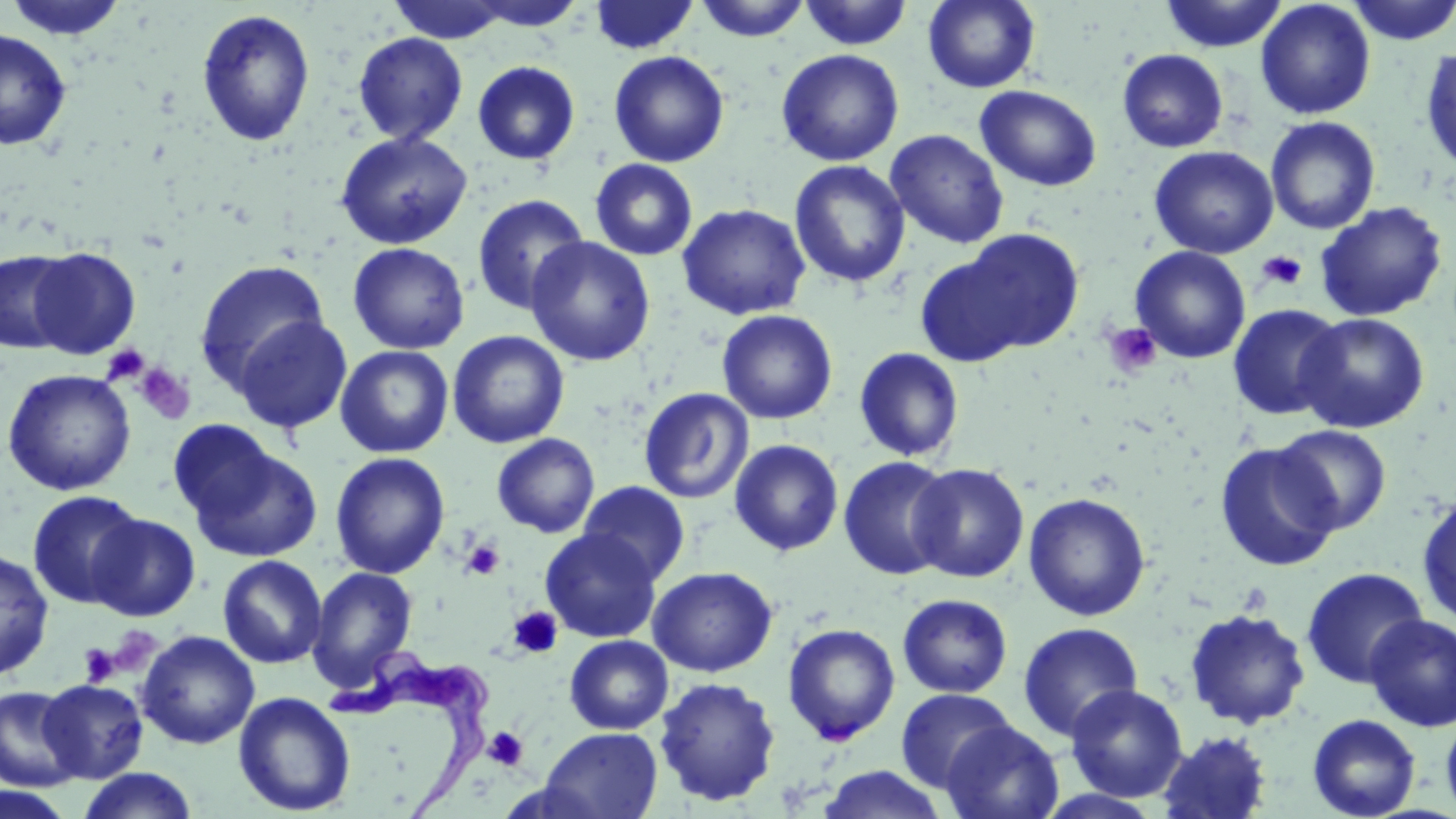

Summary:
  - Coordinate format: approximate bounding boxes as named x1/y1/x2/y2 corners in pixels
  - Platelet locations: (x1=1256, y1=250, x2=1308, y2=291), (x1=1103, y1=322, x2=1163, y2=378), (x1=102, y1=344, x2=150, y2=387), (x1=134, y1=362, x2=195, y2=424), (x1=462, y1=539, x2=504, y2=580), (x1=508, y1=606, x2=563, y2=659), (x1=106, y1=625, x2=163, y2=676), (x1=79, y1=643, x2=120, y2=686), (x1=483, y1=726, x2=529, y2=771)
  - Uninfected red blood cell locations: (x1=4, y1=0, x2=131, y2=41), (x1=386, y1=0, x2=516, y2=44), (x1=461, y1=0, x2=588, y2=31), (x1=589, y1=0, x2=700, y2=55), (x1=694, y1=0, x2=811, y2=41), (x1=798, y1=0, x2=913, y2=50), (x1=923, y1=0, x2=1040, y2=93), (x1=1159, y1=0, x2=1288, y2=53), (x1=1255, y1=0, x2=1376, y2=120), (x1=1345, y1=0, x2=1455, y2=45), (x1=196, y1=8, x2=316, y2=148), (x1=0, y1=28, x2=72, y2=151), (x1=353, y1=32, x2=467, y2=145), (x1=1420, y1=44, x2=1456, y2=174), (x1=776, y1=49, x2=904, y2=166), (x1=1117, y1=49, x2=1229, y2=152), (x1=608, y1=50, x2=729, y2=167), (x1=472, y1=61, x2=581, y2=166), (x1=975, y1=84, x2=1101, y2=192), (x1=1265, y1=117, x2=1381, y2=234), (x1=885, y1=129, x2=1009, y2=249), (x1=334, y1=130, x2=472, y2=250), (x1=1149, y1=146, x2=1279, y2=259), (x1=590, y1=158, x2=698, y2=260), (x1=789, y1=160, x2=911, y2=288), (x1=471, y1=194, x2=590, y2=316), (x1=1315, y1=201, x2=1449, y2=322), (x1=677, y1=203, x2=811, y2=320), (x1=952, y1=229, x2=1086, y2=355), (x1=526, y1=236, x2=655, y2=366), (x1=348, y1=242, x2=469, y2=354), (x1=1129, y1=245, x2=1251, y2=364), (x1=27, y1=246, x2=141, y2=359), (x1=0, y1=249, x2=75, y2=354), (x1=914, y1=252, x2=1036, y2=367), (x1=194, y1=259, x2=330, y2=392), (x1=1227, y1=304, x2=1346, y2=420), (x1=716, y1=309, x2=838, y2=424), (x1=1297, y1=312, x2=1429, y2=433), (x1=233, y1=315, x2=353, y2=434), (x1=448, y1=330, x2=570, y2=449), (x1=335, y1=344, x2=454, y2=458), (x1=853, y1=347, x2=965, y2=462), (x1=1, y1=368, x2=137, y2=496), (x1=639, y1=387, x2=754, y2=504), (x1=1273, y1=425, x2=1392, y2=534), (x1=492, y1=433, x2=599, y2=538), (x1=178, y1=434, x2=324, y2=563), (x1=729, y1=439, x2=844, y2=556), (x1=1214, y1=441, x2=1342, y2=572), (x1=330, y1=452, x2=450, y2=579), (x1=838, y1=455, x2=955, y2=580), (x1=908, y1=463, x2=1029, y2=582), (x1=578, y1=480, x2=691, y2=585), (x1=27, y1=490, x2=145, y2=609), (x1=1023, y1=492, x2=1151, y2=621), (x1=1416, y1=495, x2=1456, y2=628), (x1=88, y1=514, x2=201, y2=621), (x1=540, y1=528, x2=661, y2=643), (x1=0, y1=547, x2=54, y2=679), (x1=217, y1=554, x2=327, y2=668), (x1=307, y1=566, x2=419, y2=692), (x1=647, y1=566, x2=777, y2=677), (x1=1300, y1=566, x2=1429, y2=688), (x1=897, y1=594, x2=1013, y2=698), (x1=1184, y1=608, x2=1312, y2=729), (x1=1363, y1=614, x2=1456, y2=732), (x1=1017, y1=622, x2=1143, y2=743), (x1=782, y1=623, x2=901, y2=745), (x1=137, y1=630, x2=259, y2=749), (x1=564, y1=635, x2=673, y2=734), (x1=654, y1=676, x2=781, y2=806), (x1=38, y1=679, x2=148, y2=783), (x1=1066, y1=684, x2=1188, y2=802), (x1=0, y1=686, x2=82, y2=792), (x1=895, y1=688, x2=1016, y2=793), (x1=233, y1=691, x2=356, y2=816), (x1=1441, y1=712, x2=1456, y2=819), (x1=1307, y1=713, x2=1421, y2=819), (x1=941, y1=720, x2=1064, y2=819), (x1=539, y1=726, x2=663, y2=819), (x1=1156, y1=730, x2=1273, y2=818), (x1=815, y1=765, x2=949, y2=819), (x1=74, y1=768, x2=200, y2=819), (x1=0, y1=787, x2=77, y2=819)
  - Trypanosoma brucei locations: (x1=325, y1=645, x2=498, y2=817)
  - Slide-level diagnosis: Trypanosoma brucei
  - Field of view: single
  - Modality: light microscopy
  - Stain: May-Grünwald-Giemsa
  - Magnification: 1000x
  - Image size: 1456×819 pixels
  - Preparation: thin blood film